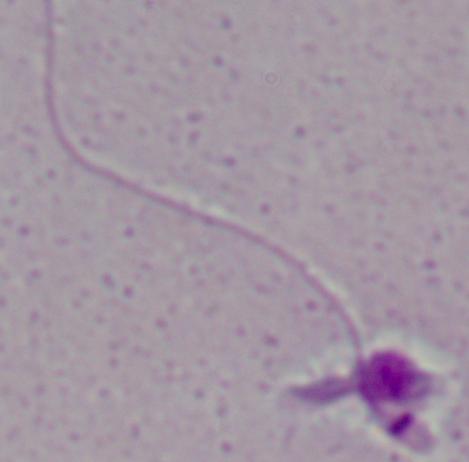
Captured at 1000x magnification. Photomicrograph. A Leishmania parasite is seen.